Locate platelets.
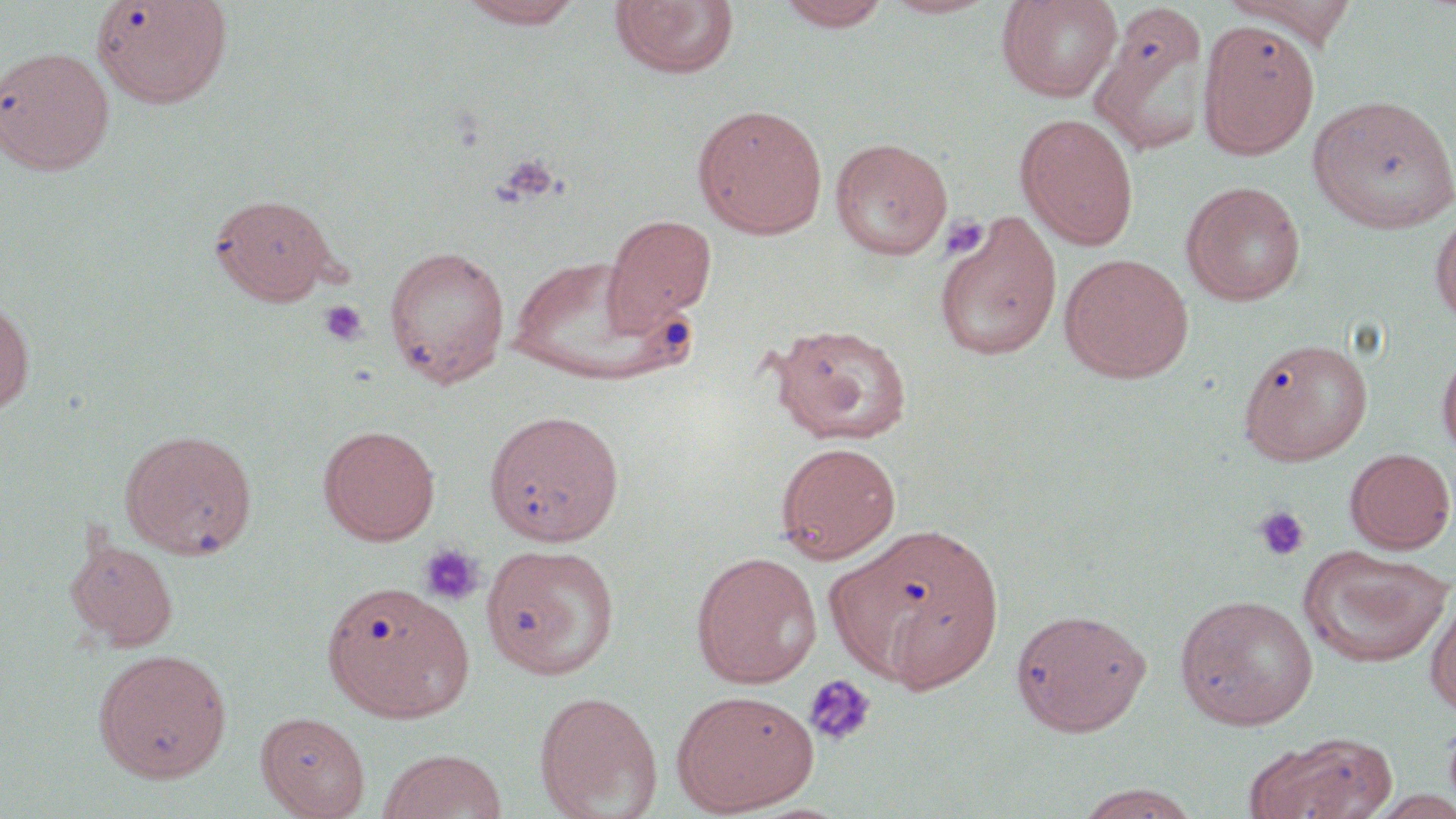
Approximate bounding boxes as (x1, y1, x2, y2) in pixels.
Platelets: (494, 153, 564, 206), (942, 213, 988, 261), (319, 300, 367, 346), (1252, 506, 1311, 562), (418, 543, 485, 605), (803, 673, 877, 748).

slide_level_diagnosis: negative for blood parasites
modality: optical microscopy
uninfected_red_blood_cell_locations: 'approximate bounding boxes as (x1, y1, x2, y2) in pixels: (92, 0, 233, 108), (455, 0, 588, 29), (774, 0, 894, 31), (877, 0, 1003, 19), (996, 0, 1122, 102), (1223, 0, 1360, 47), (610, 1, 740, 81), (1089, 5, 1213, 158), (1198, 18, 1319, 159), (1, 46, 115, 176), (1308, 94, 1456, 234), (692, 103, 828, 239), (1016, 114, 1139, 250), (829, 137, 953, 260), (1181, 180, 1306, 306), (210, 193, 339, 304), (1430, 206, 1456, 329), (935, 212, 1062, 361), (601, 214, 717, 335), (384, 245, 511, 387), (1059, 253, 1194, 382), (506, 256, 698, 385), (0, 296, 35, 416), (770, 322, 913, 446), (1237, 336, 1373, 464), (1437, 344, 1456, 461), (484, 408, 625, 546), (318, 425, 440, 544), (120, 428, 257, 560), (774, 441, 902, 563), (1344, 447, 1455, 553), (835, 523, 1005, 691), (65, 537, 179, 651), (482, 543, 620, 680), (1297, 545, 1454, 669), (691, 551, 823, 687), (321, 580, 473, 722), (1424, 585, 1456, 719), (1174, 592, 1318, 730), (1009, 606, 1153, 736), (93, 648, 232, 782), (671, 689, 818, 814), (533, 691, 662, 819), (256, 711, 370, 819), (1250, 731, 1399, 819), (376, 749, 508, 819), (1073, 783, 1202, 818)'
stain: May-Grünwald-Giemsa
image_size: 1456×819 pixels
field_of_view: one of a larger specimen
magnification: 1000x
preparation: thin blood smear